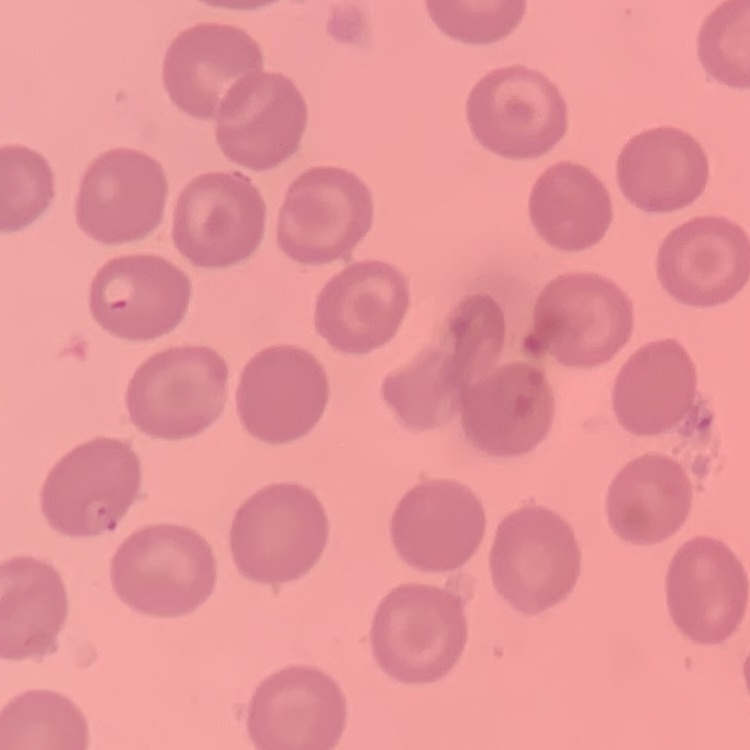

The erythrocytes show no rouleaux formation. Square crop of a larger photomicrograph. Thin blood film. Stained with either Field's or Giemsa.